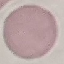

{
  "result": "no malaria parasites detected",
  "preparation": "thin blood film",
  "capture": "smartphone through the microscope eyepiece",
  "stain": "Giemsa",
  "image_type": "cell patch, automatically extracted from a larger field of view and resized to 64 × 64 pixels"
}